Locate every leukocyte (white blood cell).
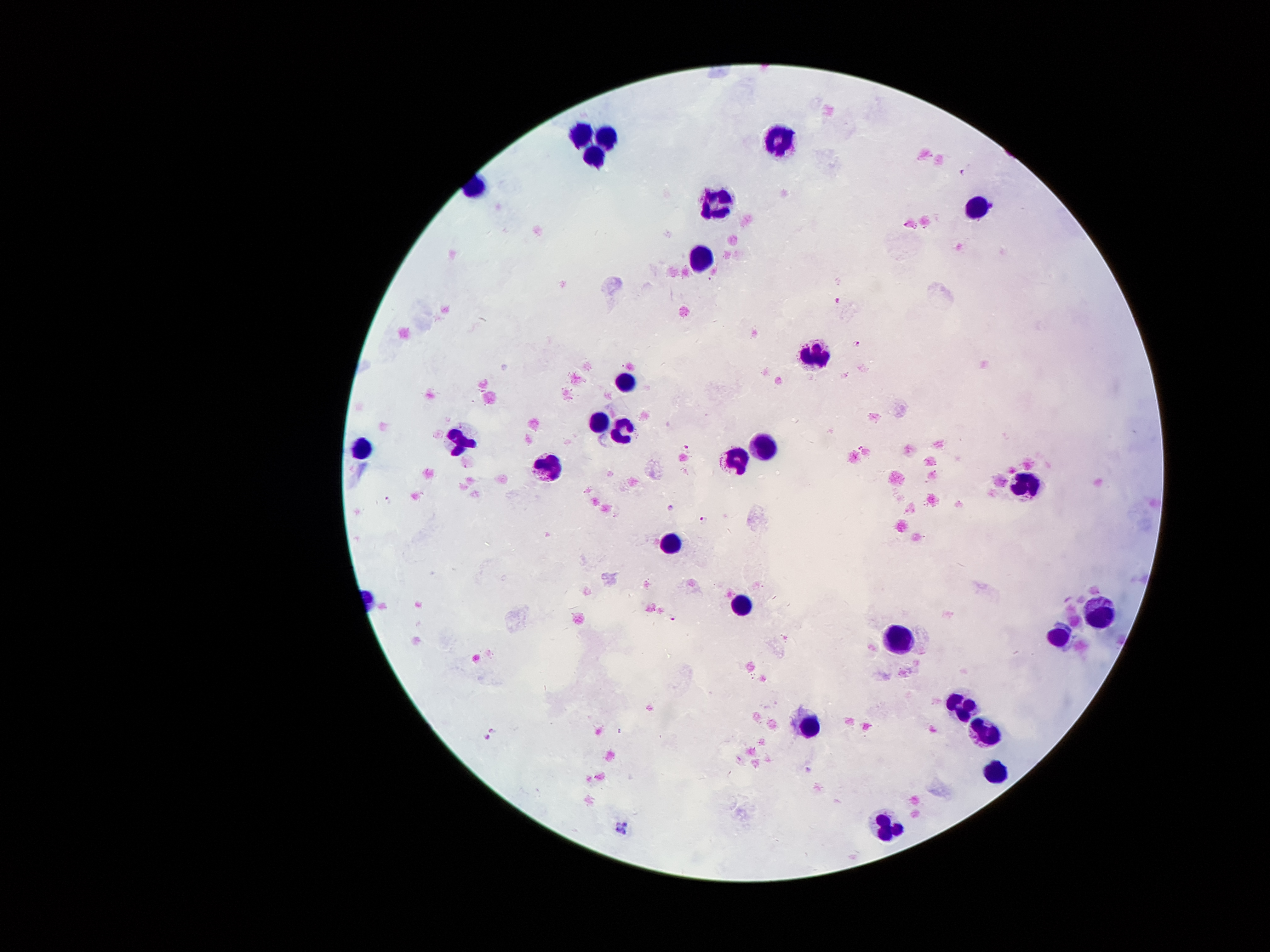

Approximate centers as (x, y) in pixels.
Leukocytes: (580, 132), (777, 136), (608, 137), (592, 159), (716, 199), (977, 204), (703, 258), (813, 354), (623, 379), (600, 420), (622, 429), (363, 446), (459, 446), (764, 447), (734, 457), (549, 467), (1030, 480), (671, 547), (740, 601), (1102, 612), (1062, 634), (900, 636), (960, 704), (811, 726), (993, 728), (995, 773), (889, 826).

Plasmodium parasite locations = (962, 170), (838, 302), (857, 345), (687, 447), (861, 447), (389, 501), (672, 508), (704, 520), (673, 617), (493, 730), (487, 738)
patient malaria status = positive for Plasmodium falciparum
image size = 1270×952 pixels
capture = smartphone through the microscope eyepiece
field of view = one from this slide
preparation = thick peripheral-blood smear
stain = Giemsa
magnification = 100x